Give the position of every malaria parasite and every leukocyte.
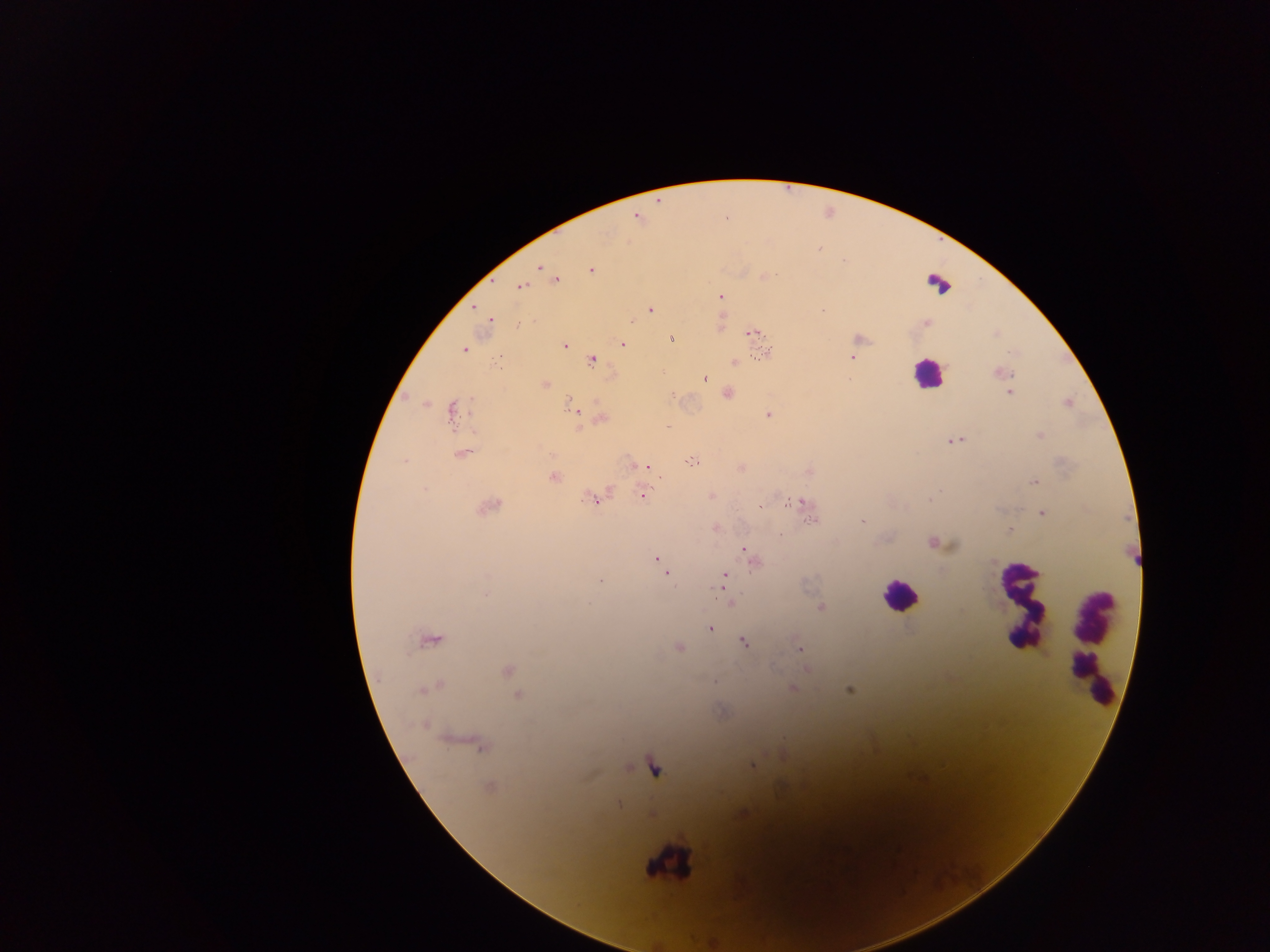

Approximate centers as x y in pixels.
Malaria parasites: 636 217; 726 217; 819 248; 539 267; 591 269; 763 276; 556 280; 521 285; 720 296; 474 307; 649 310; 822 310; 489 319; 630 320; 926 322; 753 332; 859 338; 671 339; 621 344; 564 345; 463 349; 763 352; 498 357; 852 358; 591 359; 734 360; 998 373; 704 377; 544 385; 1010 391; 726 393; 1067 402; 451 410; 574 410; 768 415; 600 418; 1041 436; 953 440; 461 453; 689 461; 632 464; 643 466; 646 466; 741 467; 808 470; 552 476; 1033 482; 642 493; 711 496; 593 498; 802 502; 487 506; 760 506; 1043 512; 862 520; 715 527; 1010 530; 780 535; 935 543; 744 550; 752 558; 656 559; 661 563; 666 573; 725 575; 600 581; 731 603; 820 607; 709 628; 430 638; 744 641; 678 647; 800 648; 805 668; 506 670; 431 686; 792 688; 850 688; 518 696; 424 725; 466 742; 480 745; 752 766; 489 787; 619 803; 743 813.
Leukocytes: 938 283; 927 375; 900 596; 1022 610; 1092 645; 667 862.
One object is labeled both malaria parasite and leukocyte by the source: 654 767.

capture = mobile-phone photograph through a microscope
field of view = single
image size = 1270×952 pixels
country = Ghana
preparation = thick blood smear